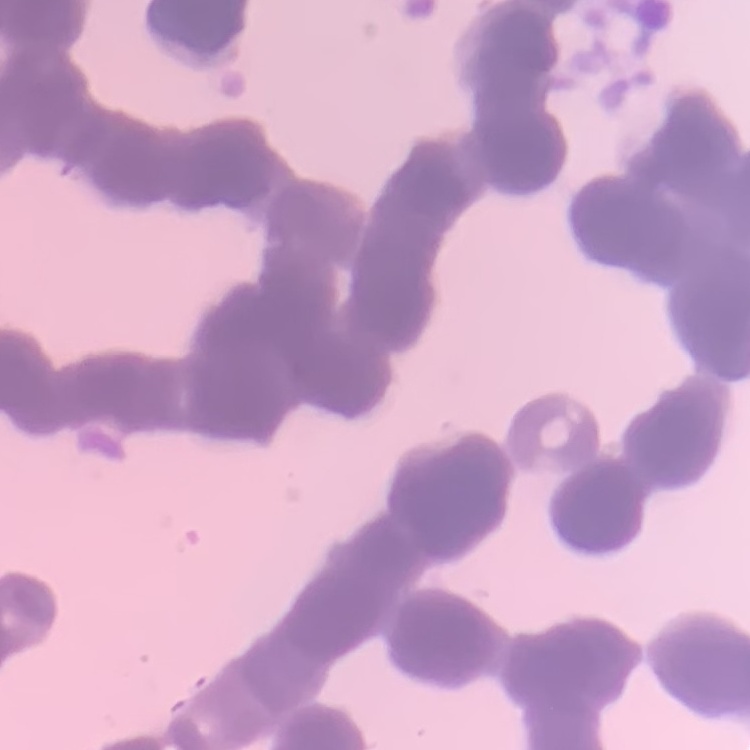
{
  "red_blood_cell_morphology": "rouleaux formation",
  "preparation": "thin blood smear",
  "stain": "Field's or Giemsa",
  "image_type": "one tile cut from a larger photomicrograph"
}